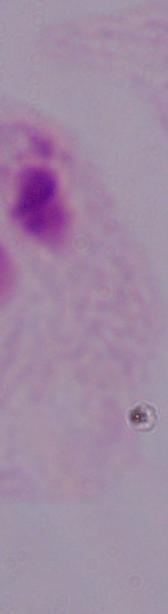
identification = trichomonad
magnification = 1000x
modality = photomicrograph